Comment on the morphology of the red blood cells.
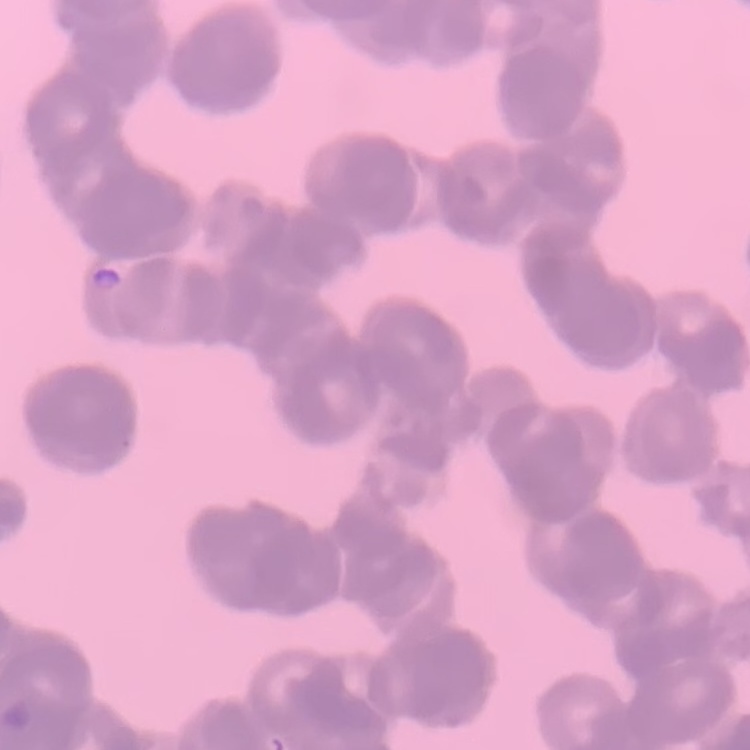
They show rouleaux formation.

Stained with either Field's or Giemsa. One tile cut from a larger photomicrograph. Thin peripheral smear.